Assess this cell for malaria.
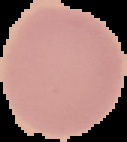

Uninfected.

Image is 127×142 pixels. Cell region segmented out of the field of view; the surrounding area is masked to black. From a thin blood smear.